Name the parasite shown.
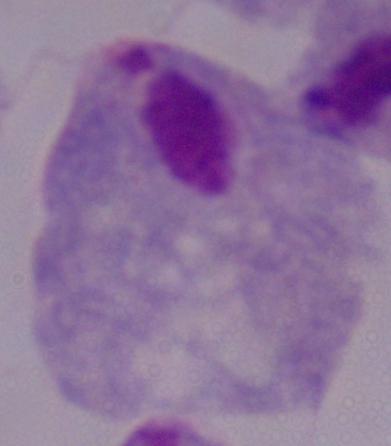

This is a trichomonad.

modality: micrograph
magnification: 1000x